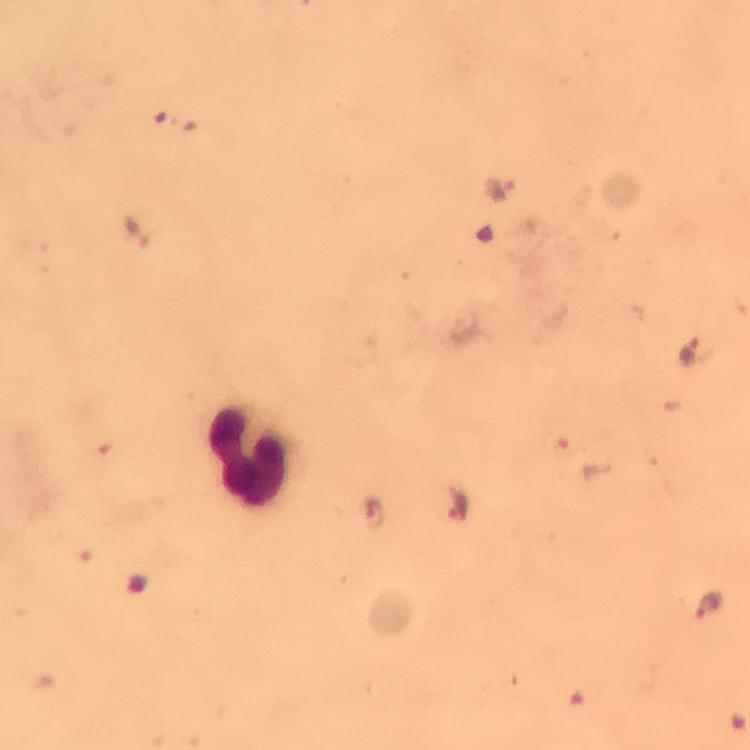

Approximate centers as (x, y) in pixels. Malaria parasite locations: (501, 190), (133, 230), (689, 349), (584, 459), (460, 502), (374, 513), (708, 605). Leukocyte locations: (252, 458). Immersion oil applied. At 100x magnification. Image is 750×750 pixels. Giemsa stain. From a diagnostic examination for malaria. Thick blood smear. Smartphone photograph taken through a microscope. Cropped region of a single field of view.